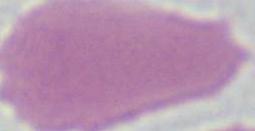
Summary:
  - Magnification: 1000x
  - Identification: erythrocyte
  - Modality: micrograph